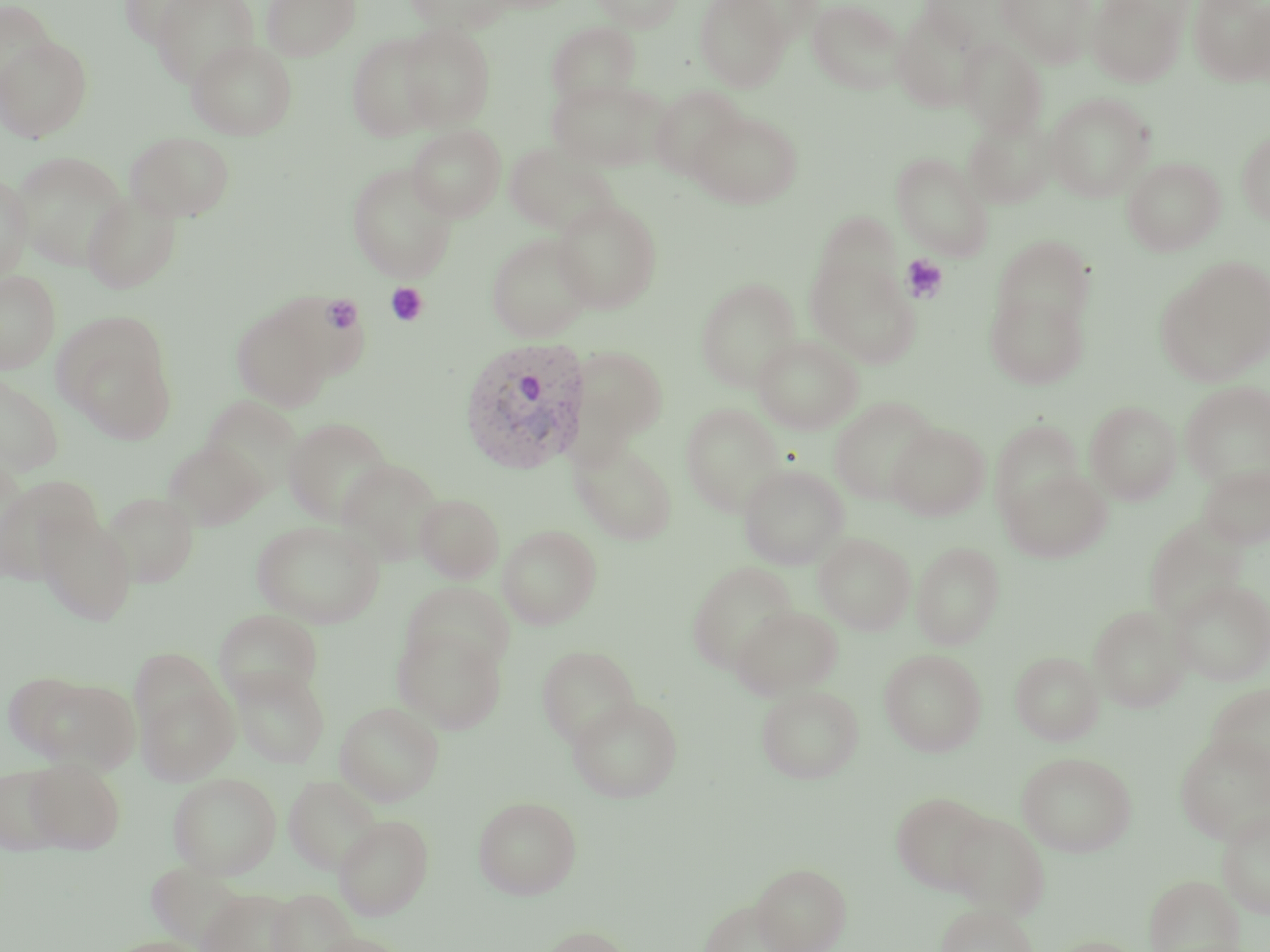
Summary:
  - Coordinate format: approximate bounding boxes as named x1/y1/x2/y2 corners in pixels
  - Uninfected red blood cell locations: (x1=119, y1=0, x2=215, y2=48), (x1=150, y1=0, x2=259, y2=88), (x1=261, y1=0, x2=360, y2=60), (x1=403, y1=0, x2=511, y2=33), (x1=592, y1=0, x2=683, y2=31), (x1=695, y1=0, x2=790, y2=91), (x1=920, y1=0, x2=1013, y2=53), (x1=998, y1=0, x2=1098, y2=68), (x1=1087, y1=0, x2=1191, y2=87), (x1=1188, y1=0, x2=1270, y2=86), (x1=727, y1=1, x2=823, y2=45), (x1=807, y1=1, x2=907, y2=94), (x1=0, y1=2, x2=59, y2=97), (x1=1236, y1=2, x2=1270, y2=85), (x1=892, y1=7, x2=984, y2=112), (x1=547, y1=22, x2=641, y2=107), (x1=399, y1=23, x2=496, y2=129), (x1=347, y1=33, x2=441, y2=142), (x1=0, y1=36, x2=93, y2=143), (x1=957, y1=38, x2=1048, y2=138), (x1=186, y1=39, x2=298, y2=140), (x1=547, y1=78, x2=669, y2=172), (x1=649, y1=86, x2=747, y2=181), (x1=1045, y1=92, x2=1155, y2=202), (x1=688, y1=111, x2=803, y2=209), (x1=963, y1=116, x2=1056, y2=209), (x1=406, y1=125, x2=507, y2=221), (x1=1236, y1=129, x2=1270, y2=225), (x1=125, y1=131, x2=236, y2=222), (x1=503, y1=142, x2=618, y2=236), (x1=11, y1=150, x2=130, y2=271), (x1=891, y1=152, x2=993, y2=260), (x1=1122, y1=157, x2=1225, y2=255), (x1=346, y1=163, x2=459, y2=282), (x1=0, y1=172, x2=33, y2=281), (x1=82, y1=191, x2=182, y2=293), (x1=551, y1=197, x2=663, y2=314), (x1=814, y1=211, x2=903, y2=300), (x1=486, y1=232, x2=595, y2=342), (x1=993, y1=235, x2=1095, y2=332), (x1=805, y1=250, x2=919, y2=367), (x1=1156, y1=257, x2=1270, y2=385), (x1=0, y1=270, x2=61, y2=374), (x1=695, y1=278, x2=801, y2=392), (x1=985, y1=289, x2=1090, y2=389), (x1=230, y1=303, x2=336, y2=412), (x1=55, y1=316, x2=175, y2=439), (x1=753, y1=335, x2=863, y2=433), (x1=568, y1=344, x2=669, y2=451), (x1=0, y1=373, x2=64, y2=476), (x1=1181, y1=381, x2=1270, y2=488), (x1=200, y1=395, x2=304, y2=497), (x1=829, y1=396, x2=941, y2=504), (x1=1085, y1=401, x2=1182, y2=504), (x1=680, y1=403, x2=786, y2=517), (x1=284, y1=417, x2=394, y2=526), (x1=990, y1=419, x2=1086, y2=522), (x1=888, y1=422, x2=989, y2=521), (x1=569, y1=438, x2=678, y2=545), (x1=163, y1=440, x2=267, y2=531), (x1=336, y1=458, x2=444, y2=565), (x1=1198, y1=463, x2=1270, y2=549), (x1=738, y1=464, x2=848, y2=569), (x1=1001, y1=466, x2=1112, y2=563), (x1=0, y1=475, x2=102, y2=586), (x1=102, y1=491, x2=199, y2=587), (x1=415, y1=494, x2=504, y2=582), (x1=36, y1=515, x2=138, y2=626), (x1=1144, y1=516, x2=1249, y2=626), (x1=252, y1=520, x2=384, y2=628), (x1=498, y1=524, x2=602, y2=629), (x1=814, y1=532, x2=915, y2=634), (x1=912, y1=541, x2=1005, y2=649), (x1=687, y1=562, x2=797, y2=672), (x1=1170, y1=578, x2=1270, y2=686), (x1=401, y1=581, x2=515, y2=677), (x1=1088, y1=604, x2=1190, y2=712), (x1=730, y1=605, x2=843, y2=699), (x1=213, y1=609, x2=323, y2=704), (x1=393, y1=624, x2=507, y2=733), (x1=537, y1=644, x2=640, y2=746), (x1=879, y1=649, x2=986, y2=756), (x1=1010, y1=651, x2=1104, y2=745), (x1=230, y1=666, x2=330, y2=768), (x1=19, y1=674, x2=140, y2=772), (x1=136, y1=680, x2=239, y2=785), (x1=1205, y1=683, x2=1270, y2=780), (x1=756, y1=685, x2=864, y2=783), (x1=567, y1=696, x2=683, y2=802), (x1=335, y1=701, x2=444, y2=805), (x1=1175, y1=734, x2=1270, y2=844), (x1=1016, y1=751, x2=1137, y2=856), (x1=25, y1=757, x2=126, y2=854), (x1=0, y1=765, x2=67, y2=853), (x1=168, y1=772, x2=282, y2=879), (x1=283, y1=775, x2=383, y2=874), (x1=890, y1=792, x2=994, y2=894), (x1=473, y1=795, x2=582, y2=899), (x1=1216, y1=807, x2=1270, y2=918), (x1=946, y1=812, x2=1050, y2=918), (x1=333, y1=815, x2=434, y2=920), (x1=146, y1=862, x2=248, y2=949), (x1=751, y1=862, x2=851, y2=952), (x1=1145, y1=874, x2=1245, y2=952), (x1=198, y1=888, x2=301, y2=952), (x1=268, y1=888, x2=358, y2=952), (x1=698, y1=898, x2=800, y2=951), (x1=935, y1=902, x2=1039, y2=952), (x1=536, y1=925, x2=636, y2=952), (x1=307, y1=932, x2=413, y2=952), (x1=1042, y1=936, x2=1150, y2=952), (x1=107, y1=937, x2=209, y2=952)
  - Plasmodium vivax-infected red blood cell locations: (x1=459, y1=337, x2=592, y2=474)
  - Platelet locations: (x1=901, y1=255, x2=948, y2=303), (x1=385, y1=282, x2=428, y2=326), (x1=322, y1=295, x2=363, y2=334)
  - Slide-level diagnosis: Plasmodium vivax
  - Field of view: single
  - Image size: 1270×952 pixels
  - Stain: May-Grünwald-Giemsa
  - Magnification: 1000x
  - Modality: light microscopy
  - Preparation: thin blood film